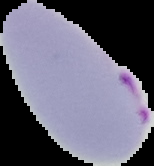
From a thin blood smear. Image is 154×166 pixels. Result: malaria parasites identified. Segmented cell region on a black background.